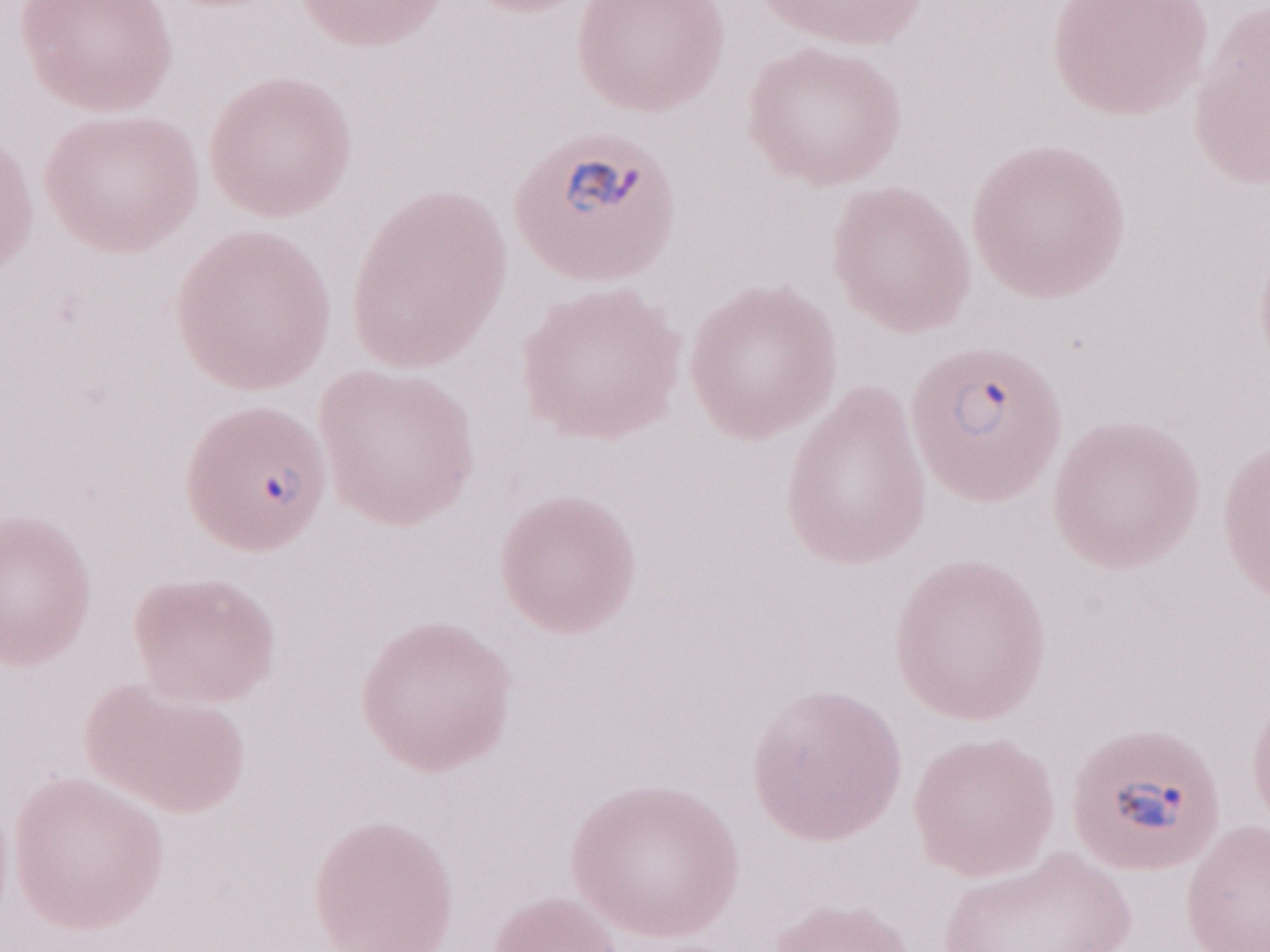

Patient-level malaria diagnosis: positive. Thin peripheral-blood smear. Olympus BX43 microscope and DP73 digital camera. Image is 1270×952 pixels. May-Grünwald-Giemsa stain. Single field of view. Magnification: 1,000x.